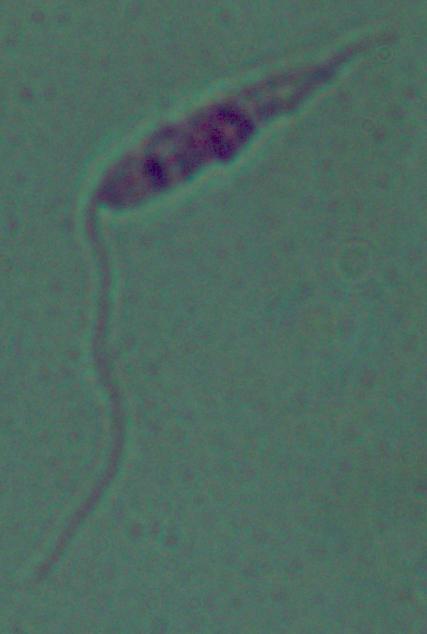
modality = photomicrograph
identification = Leishmania
magnification = 1000x